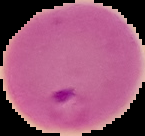
preparation = thin blood smear
result = Plasmodium parasites identified
image type = segmented cell region with the area outside set to black
image size = 145×136 pixels